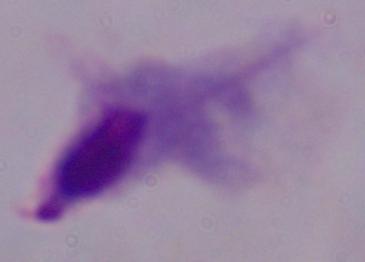
{
  "magnification": "1000x",
  "identification": "trichomonad",
  "modality": "micrograph"
}